Give the position of every Plasmodium parasite.
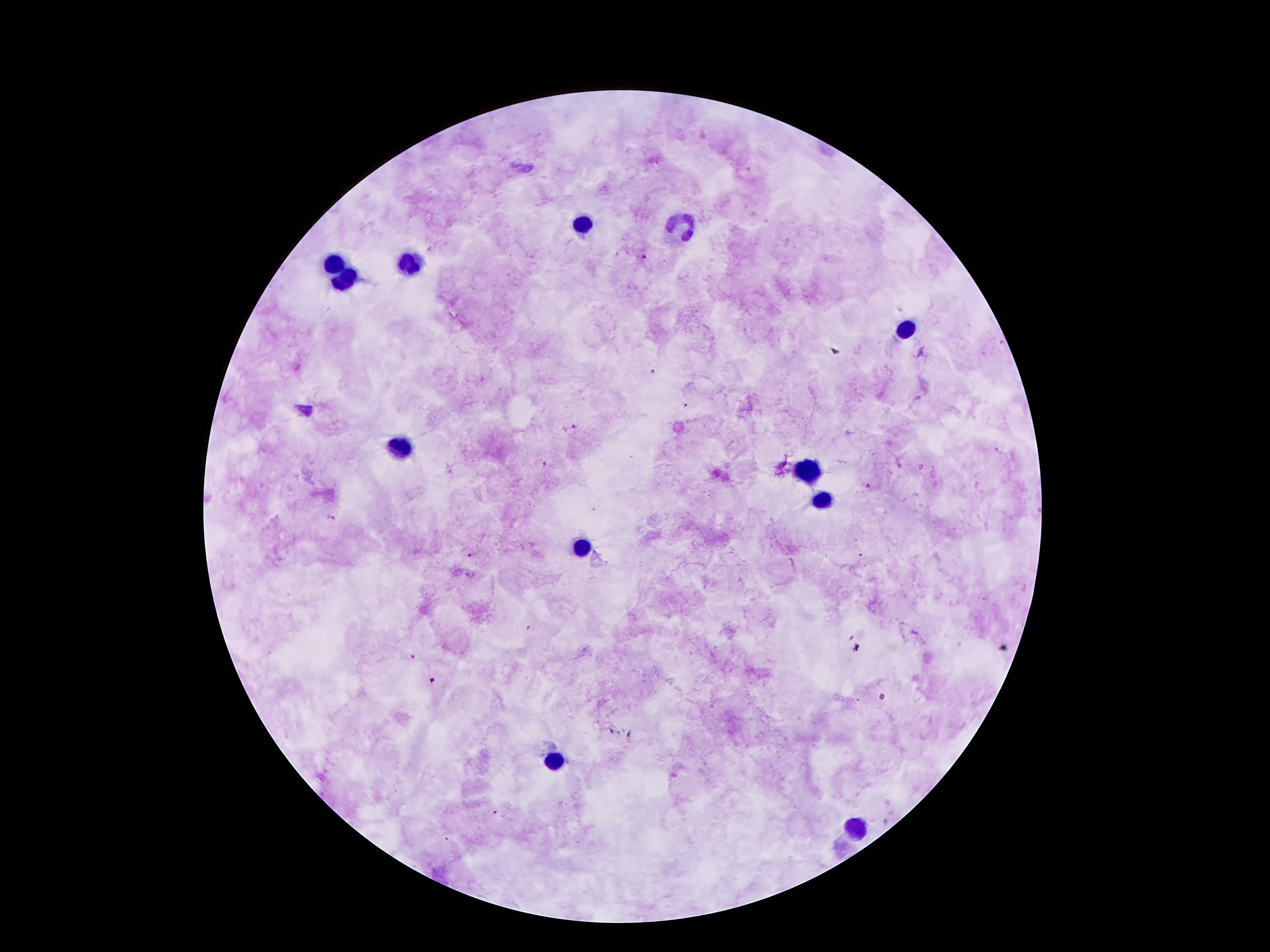
Approximate centers as {x, y} in pixels.
Plasmodium parasites: {643, 258}, {651, 372}, {687, 405}, {577, 427}, {544, 464}, {869, 486}, {332, 519}, {861, 555}, {468, 556}, {528, 629}, {413, 658}, {433, 680}, {495, 812}, {446, 839}.

Summary:
  - Leukocyte locations: {585, 222}, {683, 225}, {407, 263}, {333, 264}, {345, 278}, {903, 332}, {402, 449}, {806, 468}, {819, 500}, {581, 548}, {552, 761}, {858, 828}
  - Field of view: single
  - Stain: Giemsa
  - Capture: smartphone camera through the microscope eyepiece
  - Magnification: 100x
  - Preparation: thick blood film
  - Patient malaria status: infected with Plasmodium falciparum
  - Image size: 1270×952 pixels